Locate every blood parasite and identify its species.
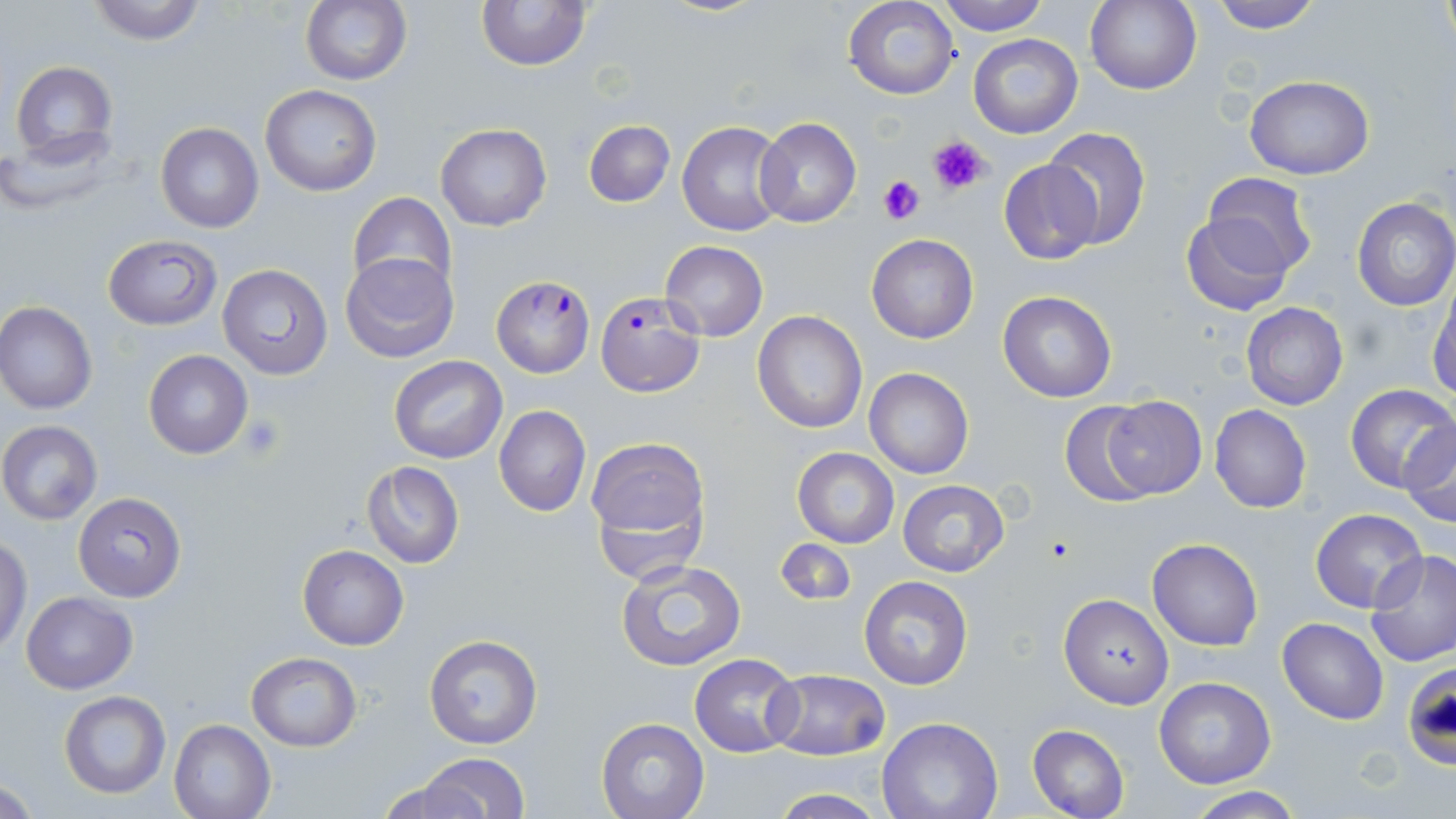

Approximate bounding boxes as (x1, y1, x2, y2) in pixels.
Plasmodium falciparum-infected red blood cells: (491, 276, 596, 378), (595, 292, 705, 398).
No Plasmodium ovale, Plasmodium malariae, Plasmodium vivax, Babesia divergens, or Trypanosoma brucei observed.

slide-level diagnosis = Plasmodium falciparum
preparation = thin blood smear
stain = May-Grünwald-Giemsa
platelet locations = approximate bounding boxes as (x1, y1, x2, y2) in pixels: (927, 133, 991, 196), (880, 175, 927, 226), (239, 415, 287, 462)
field of view = single
image size = 1456×819 pixels
uninfected red blood cell locations = approximate bounding boxes as (x1, y1, x2, y2) in pixels: (83, 0, 210, 44), (300, 0, 413, 87), (934, 0, 1050, 35), (1086, 0, 1201, 94), (1208, 0, 1325, 32), (1438, 0, 1454, 55), (475, 1, 591, 72), (843, 2, 961, 101), (968, 34, 1083, 139), (9, 60, 118, 162), (1245, 74, 1375, 180), (260, 85, 383, 196), (583, 119, 675, 208), (754, 119, 860, 229), (676, 121, 788, 236), (155, 122, 265, 233), (435, 123, 553, 232), (0, 127, 126, 215), (1042, 128, 1151, 250), (998, 158, 1101, 265), (1201, 172, 1317, 278), (347, 192, 457, 297), (1352, 197, 1456, 311), (1182, 208, 1297, 313), (867, 233, 978, 343), (102, 235, 221, 330), (660, 242, 768, 342), (339, 250, 460, 365), (217, 263, 333, 380), (1428, 282, 1456, 401), (997, 291, 1116, 403), (0, 301, 97, 414), (1241, 301, 1347, 411), (752, 311, 868, 433), (143, 349, 254, 458), (388, 355, 507, 464), (864, 368, 973, 479), (1344, 384, 1456, 495), (1102, 395, 1207, 499), (1059, 398, 1165, 507), (493, 405, 590, 517), (1210, 405, 1311, 513), (1, 421, 102, 524), (1400, 421, 1456, 526), (585, 436, 709, 562), (791, 447, 899, 548), (361, 462, 464, 567), (897, 478, 1010, 579), (73, 492, 187, 602), (1310, 507, 1427, 612), (1147, 537, 1264, 651), (0, 538, 31, 653), (774, 538, 855, 606), (297, 543, 408, 651), (1366, 549, 1456, 666), (616, 560, 747, 671), (859, 575, 973, 691), (20, 592, 137, 693), (1057, 593, 1175, 709), (1277, 617, 1389, 724), (422, 635, 543, 751), (246, 652, 362, 750), (690, 653, 802, 756), (766, 670, 890, 759), (1152, 677, 1276, 789), (58, 690, 170, 800), (595, 717, 709, 818), (875, 717, 1003, 819), (169, 719, 275, 819), (1027, 724, 1129, 819), (417, 753, 531, 819), (370, 774, 494, 818), (2, 776, 42, 817), (1186, 789, 1307, 819), (765, 791, 891, 819)
modality = light microscopy
magnification = 1000x